Identify the cell.
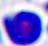

A leukocyte.

Summary:
  - Magnification: 400x
  - Modality: micrograph